Locate and identify every blood parasite.
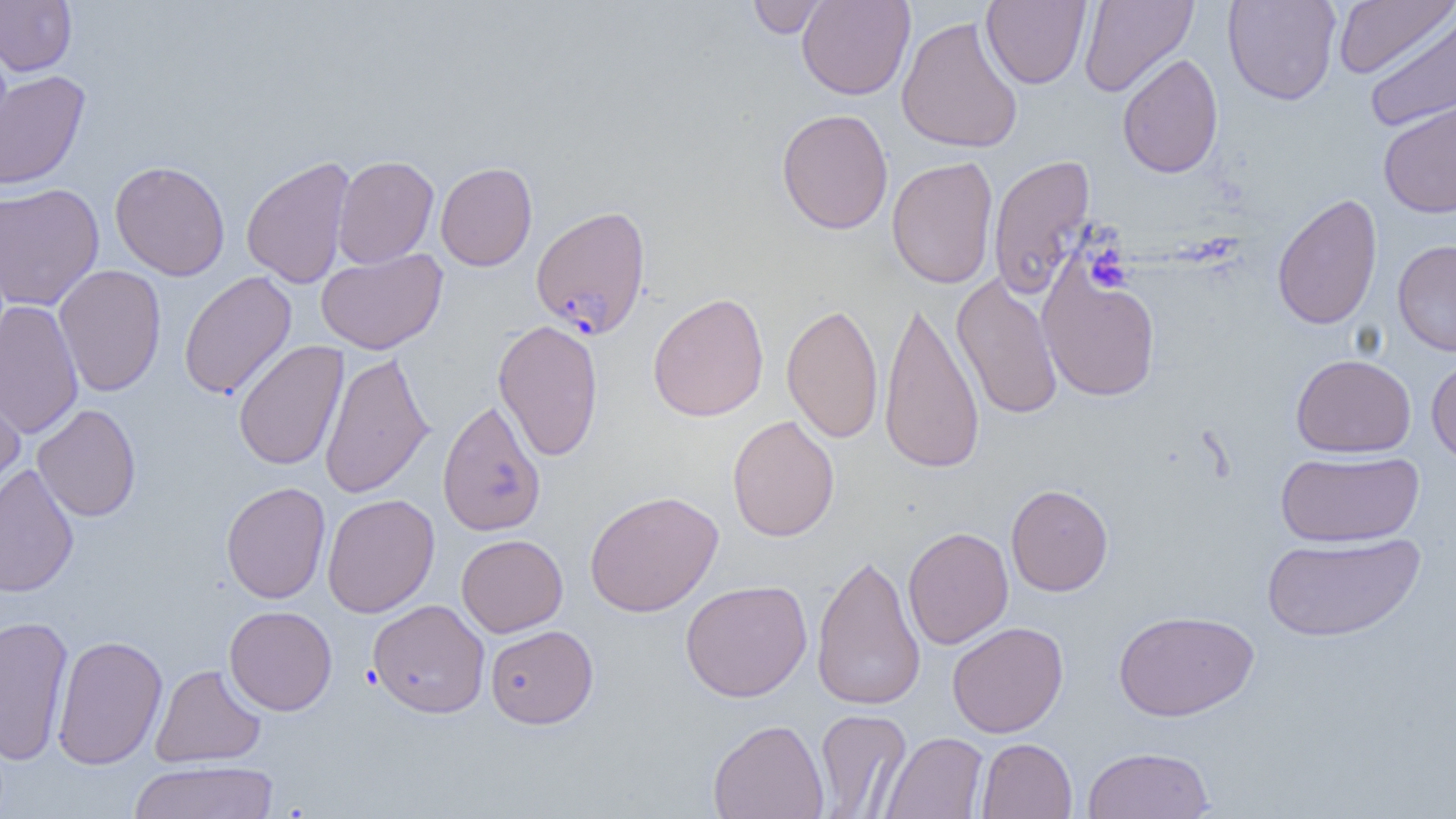
Approximate bounding boxes as [x1, y1, x2, y2] in pixels.
Plasmodium falciparum-infected red blood cells: [530, 204, 651, 339].
No Plasmodium ovale, Plasmodium malariae, Plasmodium vivax, Babesia divergens, or Trypanosoma brucei observed.

Platelet locations: [1085, 244, 1132, 293]. Uninfected red blood cell locations: [0, 0, 77, 76], [746, 0, 830, 38], [796, 0, 915, 100], [981, 0, 1091, 89], [1078, 0, 1198, 98], [1222, 0, 1342, 106], [1332, 0, 1454, 79], [1363, 8, 1456, 133], [896, 16, 1024, 154], [1117, 53, 1224, 178], [0, 70, 91, 190], [1378, 99, 1456, 218], [776, 108, 894, 235], [987, 154, 1096, 299], [241, 155, 356, 289], [333, 155, 439, 269], [886, 156, 999, 289], [110, 160, 230, 281], [435, 161, 537, 271], [0, 183, 104, 311], [1271, 193, 1382, 330], [1392, 238, 1456, 356], [316, 249, 447, 354], [53, 264, 166, 397], [1038, 265, 1161, 402], [178, 271, 297, 400], [951, 273, 1063, 421], [648, 292, 769, 422], [878, 298, 984, 476], [0, 299, 84, 439], [781, 302, 883, 444], [493, 318, 604, 462], [233, 340, 348, 471], [319, 350, 434, 499], [1291, 353, 1416, 457], [1425, 355, 1456, 467], [0, 372, 25, 500], [437, 398, 547, 537], [32, 404, 142, 522], [727, 415, 840, 542], [1275, 450, 1424, 547], [0, 465, 79, 598], [220, 481, 331, 604], [1006, 483, 1113, 596], [584, 490, 723, 617], [322, 493, 440, 617], [902, 526, 1014, 649], [1261, 531, 1425, 642], [456, 534, 568, 637], [810, 551, 925, 712], [680, 579, 812, 702], [367, 599, 490, 718], [224, 605, 337, 716], [1113, 609, 1259, 721], [0, 615, 74, 765], [947, 621, 1068, 738], [485, 624, 598, 729], [52, 634, 167, 769], [151, 663, 266, 767], [813, 709, 911, 817], [708, 718, 829, 819], [880, 731, 989, 819], [976, 737, 1077, 818], [1082, 746, 1215, 818], [127, 760, 280, 818]. Slide-level diagnosis: Plasmodium falciparum. Thin blood smear. 1000x magnification. Single field of view. Light microscopy. Image is 1456×819 pixels.